Classify this cell by malaria status.
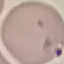

Parasitized.

image type = automatically extracted cell patch, resized to 64 × 64 pixels
preparation = thin blood film
capture = smartphone through the microscope eyepiece
stain = Giemsa